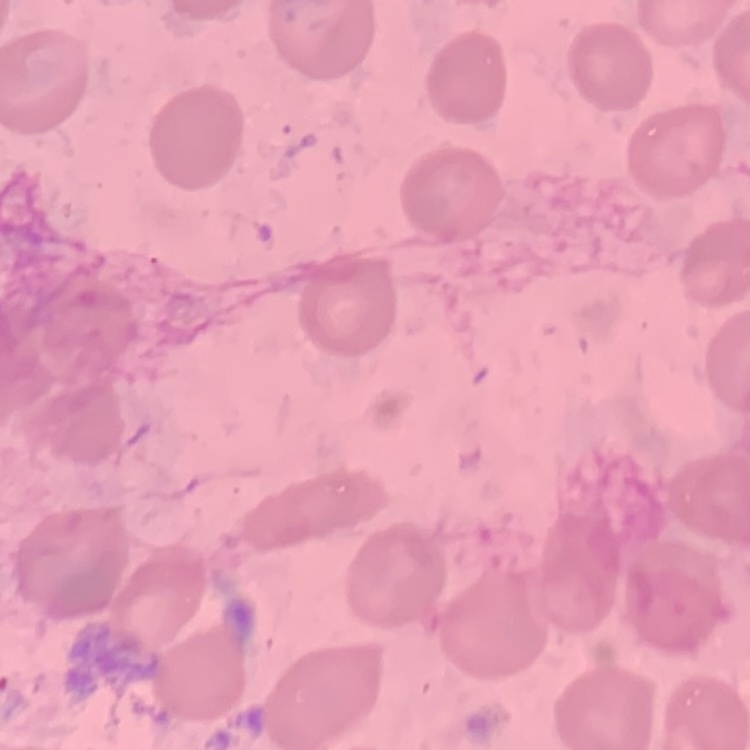
red blood cell morphology = no rouleaux formation
stain = Field's or Giemsa
image type = square crop of a larger photomicrograph
preparation = thin blood film